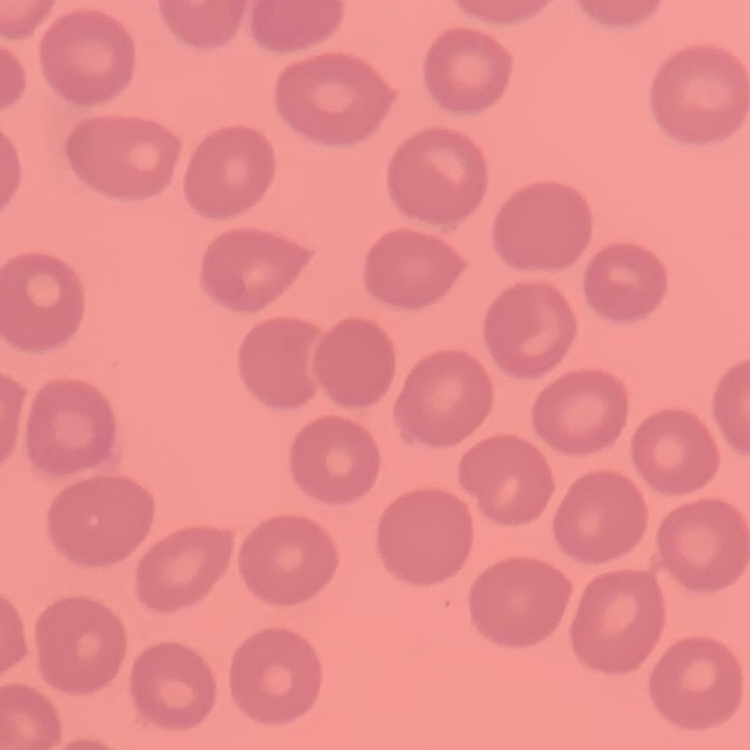 The erythrocytes exhibit no rouleaux formation. Thin blood film. Square crop of a larger photomicrograph. Field's or Giemsa stain.